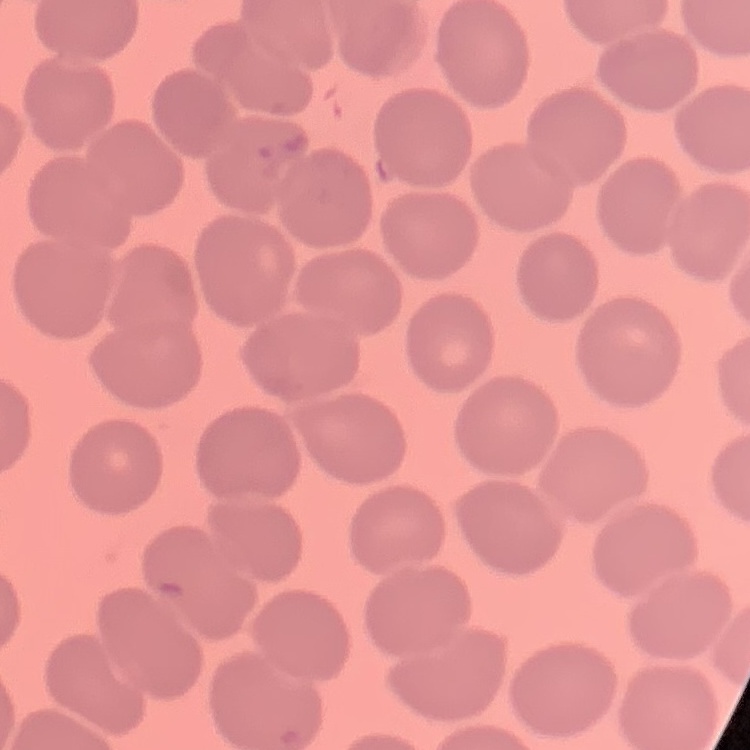 The erythrocytes show no rouleaux formation. One tile cut from a larger photomicrograph. Stained with either Field's or Giemsa. Thin peripheral smear.